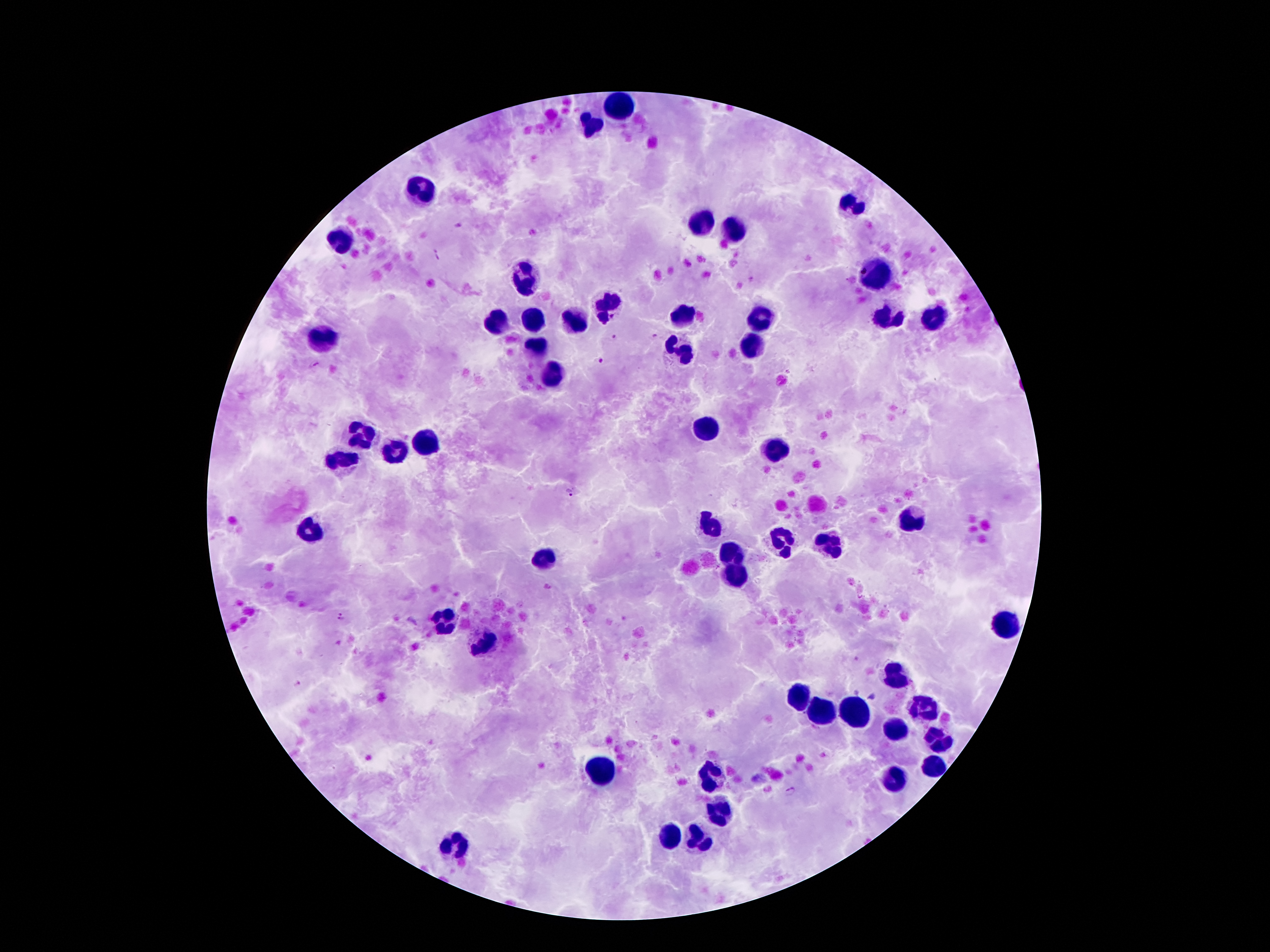

Approximate centers as (x, y) in pixels.
Summary:
  - Leukocyte locations: (614, 102), (590, 123), (420, 191), (851, 202), (701, 224), (732, 233), (342, 240), (878, 275), (524, 279), (607, 304), (678, 316), (930, 318), (888, 319), (762, 320), (530, 321), (495, 323), (574, 324), (325, 337), (753, 346), (539, 349), (678, 353), (553, 377), (704, 428), (357, 437), (425, 443), (775, 449), (396, 455), (341, 462), (909, 521), (704, 526), (309, 528), (778, 540), (828, 544), (729, 551), (541, 561), (733, 577), (437, 622), (1002, 624), (486, 643), (897, 677), (799, 696), (924, 706), (822, 713), (854, 713), (894, 729), (936, 740), (933, 764), (600, 771), (707, 780), (891, 781), (720, 808), (668, 838), (701, 839), (455, 845)
  - Plasmodium parasite locations: (437, 253), (656, 337), (615, 340), (600, 360), (571, 494), (341, 618), (297, 685), (870, 696), (791, 788)
  - Field of view: one from this slide
  - Image size: 1270×952 pixels
  - Capture: smartphone through the microscope eyepiece
  - Patient malaria status: infected with Plasmodium falciparum
  - Stain: Giemsa
  - Magnification: 100x
  - Preparation: thick blood smear